Identify the parasite.
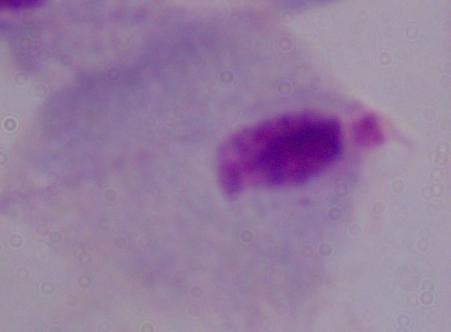
This is a trichomonad.

modality = micrograph
magnification = 1000x